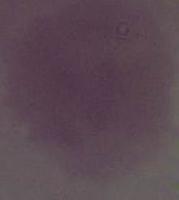
Photomicrograph. A red blood cell is seen. 1000x magnification.